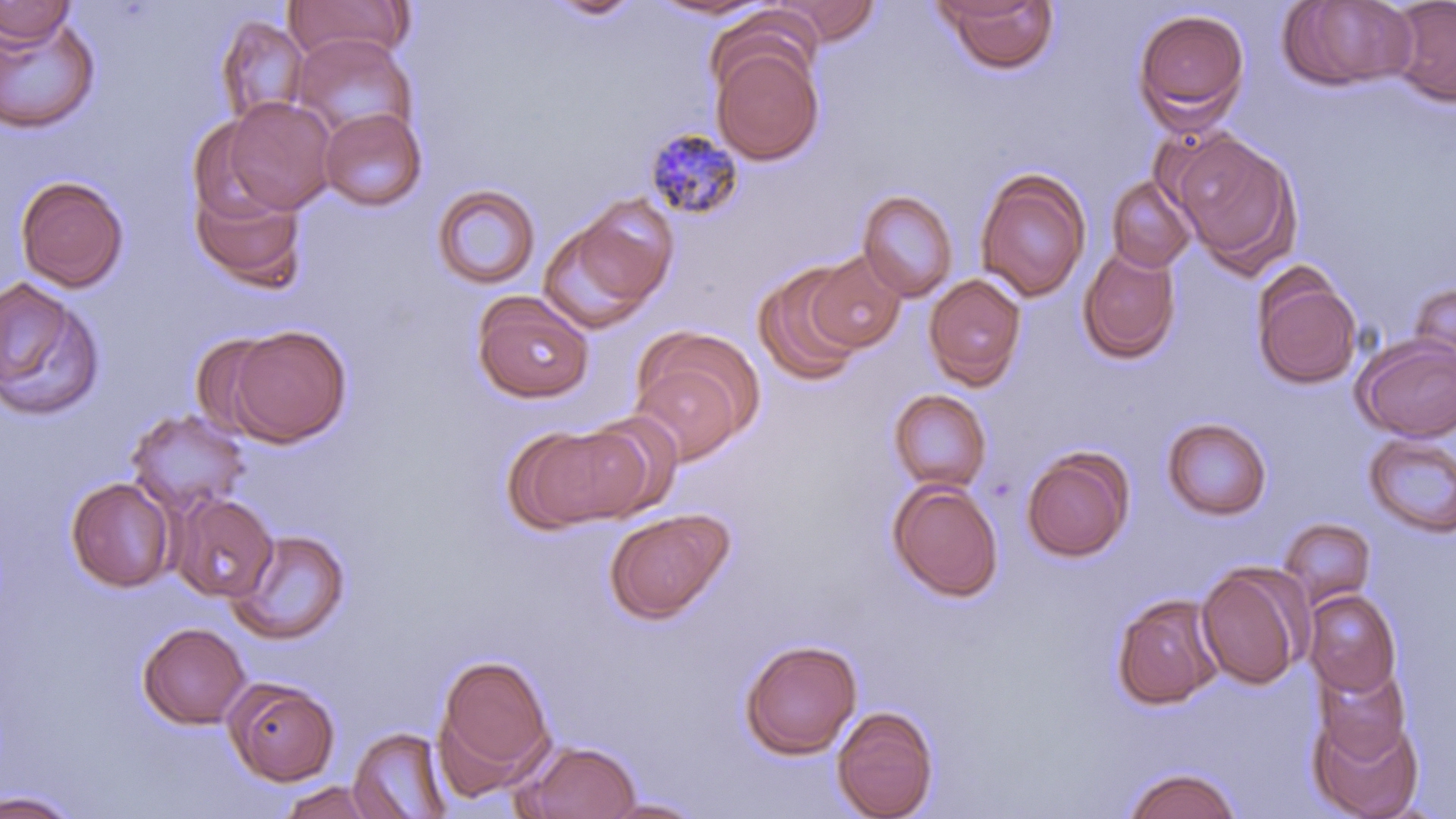
Summary:
  - Coordinate format: approximate bounding boxes as (x1, y1, x2, y2) in pixels
  - Uninfected red blood cell locations: (281, 0, 414, 64), (545, 0, 646, 22), (1278, 0, 1417, 92), (1387, 0, 1456, 107), (0, 1, 76, 47), (645, 1, 776, 20), (770, 1, 882, 46), (938, 1, 1061, 75), (1133, 8, 1250, 132), (0, 11, 101, 134), (214, 15, 310, 127), (288, 33, 416, 141), (710, 41, 825, 165), (222, 97, 336, 213), (319, 107, 427, 212), (187, 119, 287, 227), (1170, 130, 1302, 274), (975, 170, 1090, 302), (15, 175, 129, 292), (1106, 176, 1196, 274), (190, 180, 308, 292), (432, 183, 542, 291), (857, 190, 959, 302), (539, 206, 673, 333), (1078, 246, 1182, 363), (806, 252, 906, 352), (1251, 266, 1362, 390), (752, 268, 864, 390), (923, 273, 1027, 390), (0, 276, 105, 422), (1408, 281, 1456, 383), (471, 290, 595, 403), (224, 324, 352, 447), (638, 327, 764, 439), (190, 333, 286, 439), (1353, 335, 1456, 442), (629, 362, 744, 466), (888, 389, 992, 493), (125, 408, 252, 518), (576, 411, 684, 519), (1161, 416, 1273, 521), (507, 423, 649, 532), (1362, 433, 1456, 538), (1020, 447, 1134, 563), (65, 477, 177, 593), (887, 479, 1003, 602), (172, 493, 278, 602), (603, 507, 735, 623), (1278, 518, 1377, 608), (226, 528, 352, 645), (1195, 564, 1308, 690), (1303, 589, 1402, 697), (1110, 592, 1225, 711), (137, 622, 251, 729), (739, 638, 863, 759), (435, 653, 555, 786), (1314, 665, 1412, 762), (224, 678, 339, 786), (831, 704, 939, 819), (1308, 711, 1424, 819), (348, 726, 452, 819), (520, 739, 642, 819), (1120, 765, 1244, 818), (275, 779, 391, 818), (0, 788, 84, 818), (597, 796, 709, 818)
  - Plasmodium malariae-infected red blood cell locations: (644, 128, 745, 221)
  - Slide-level diagnosis: Plasmodium malariae
  - Preparation: thin blood smear
  - Stain: May-Grünwald-Giemsa
  - Magnification: 1000x
  - Field of view: single
  - Image size: 1456×819 pixels
  - Modality: light microscopy